Assess the morphology of the red blood cells.
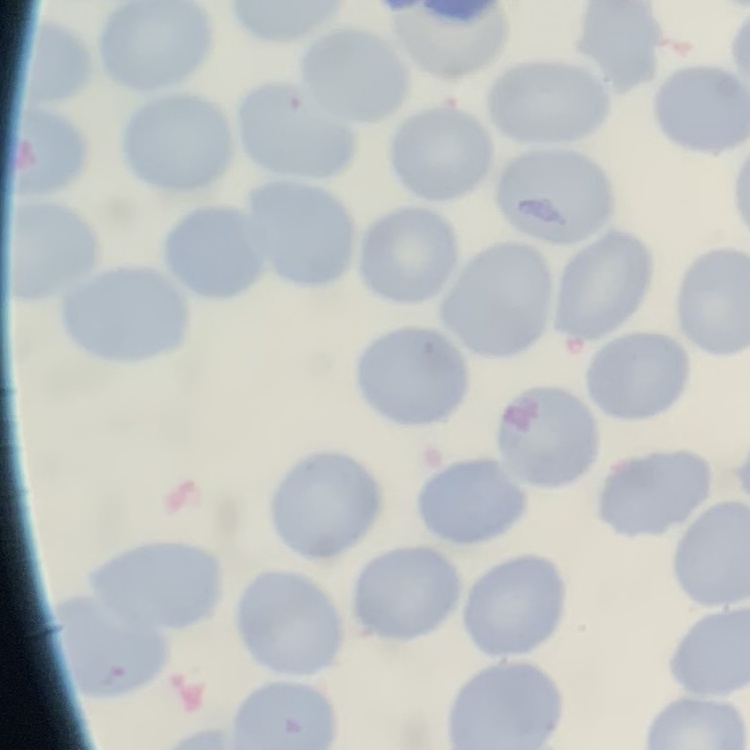
They show no rouleaux formation.

preparation = thin peripheral smear
stain = Field's or Giemsa
image type = one tile cut from a larger photomicrograph